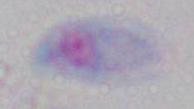

magnification = 1000x
modality = photomicrograph
identification = Toxoplasma gondii